Locate and identify every blood parasite.
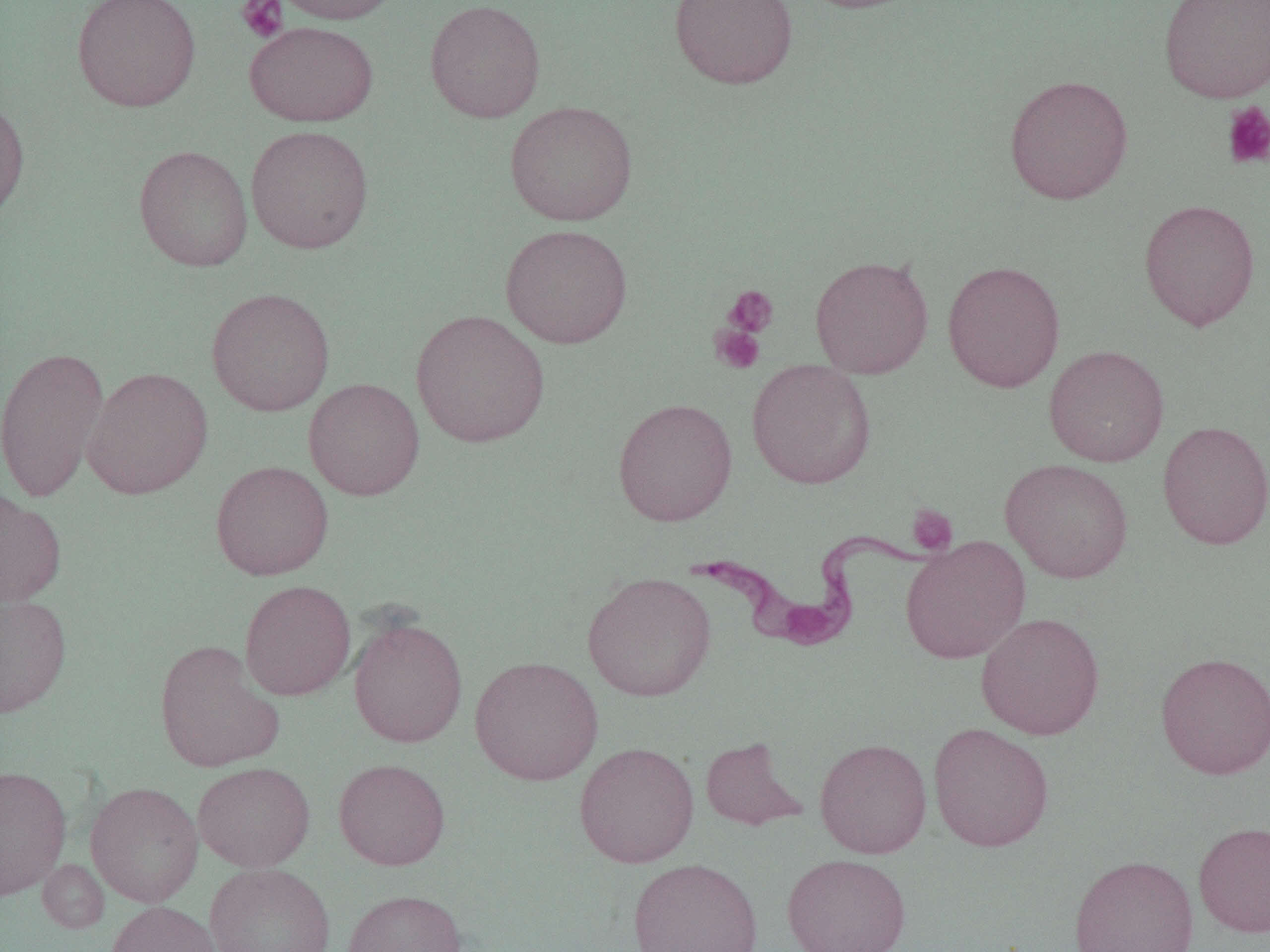

Approximate bounding boxes as [x1, y1, x2, y2] in pixels.
Trypanosoma brucei: [687, 528, 935, 648].
No Plasmodium falciparum, Plasmodium ovale, Plasmodium malariae, Plasmodium vivax, or Babesia divergens observed.

Summary:
  - Platelet locations: [235, 0, 289, 43], [1221, 101, 1270, 171], [723, 285, 779, 339], [710, 323, 765, 375], [906, 504, 957, 555]
  - Uninfected red blood cell locations: [71, 0, 202, 112], [270, 0, 406, 25], [424, 0, 546, 123], [668, 0, 798, 89], [794, 0, 929, 14], [1158, 0, 1270, 103], [244, 20, 379, 127], [1004, 74, 1134, 205], [0, 93, 30, 225], [504, 100, 638, 226], [245, 125, 374, 254], [133, 144, 253, 271], [1139, 198, 1260, 330], [500, 224, 633, 348], [809, 255, 934, 378], [942, 260, 1065, 393], [205, 287, 336, 416], [410, 309, 549, 448], [0, 345, 110, 502], [1044, 345, 1169, 467], [747, 359, 877, 490], [82, 366, 213, 499], [303, 378, 425, 500], [612, 397, 738, 526], [1157, 421, 1270, 550], [1000, 458, 1134, 583], [211, 460, 334, 580], [0, 488, 67, 608], [899, 535, 1031, 664], [582, 572, 716, 702], [240, 579, 356, 700], [0, 593, 72, 719], [976, 612, 1105, 740], [348, 615, 468, 747], [154, 640, 284, 773], [1155, 651, 1270, 779], [470, 655, 603, 785], [928, 722, 1054, 852], [700, 736, 807, 831], [814, 738, 932, 858], [573, 741, 699, 868], [333, 758, 451, 870], [192, 762, 315, 872], [0, 766, 72, 901], [85, 781, 204, 907], [1193, 820, 1270, 937], [781, 853, 912, 952], [1069, 854, 1199, 952], [627, 857, 763, 952], [38, 859, 109, 933], [204, 862, 337, 952], [342, 889, 467, 952], [106, 900, 221, 952]
  - Slide-level diagnosis: Trypanosoma brucei
  - Modality: optical microscopy
  - Image size: 1270×952 pixels
  - Preparation: thin blood film
  - Field of view: one of a larger specimen
  - Magnification: 1000x